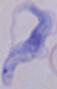

Summary:
  - Identification: trypanosome
  - Magnification: 1000x
  - Modality: micrograph